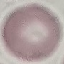
Summary:
  - Result: no malaria parasites seen
  - Preparation: thin blood smear
  - Capture: smartphone camera at the microscope eyepiece
  - Image type: cell patch, automatically extracted from a larger field of view and resized to 64 × 64 pixels
  - Stain: Giemsa